Name the blood parasite species.
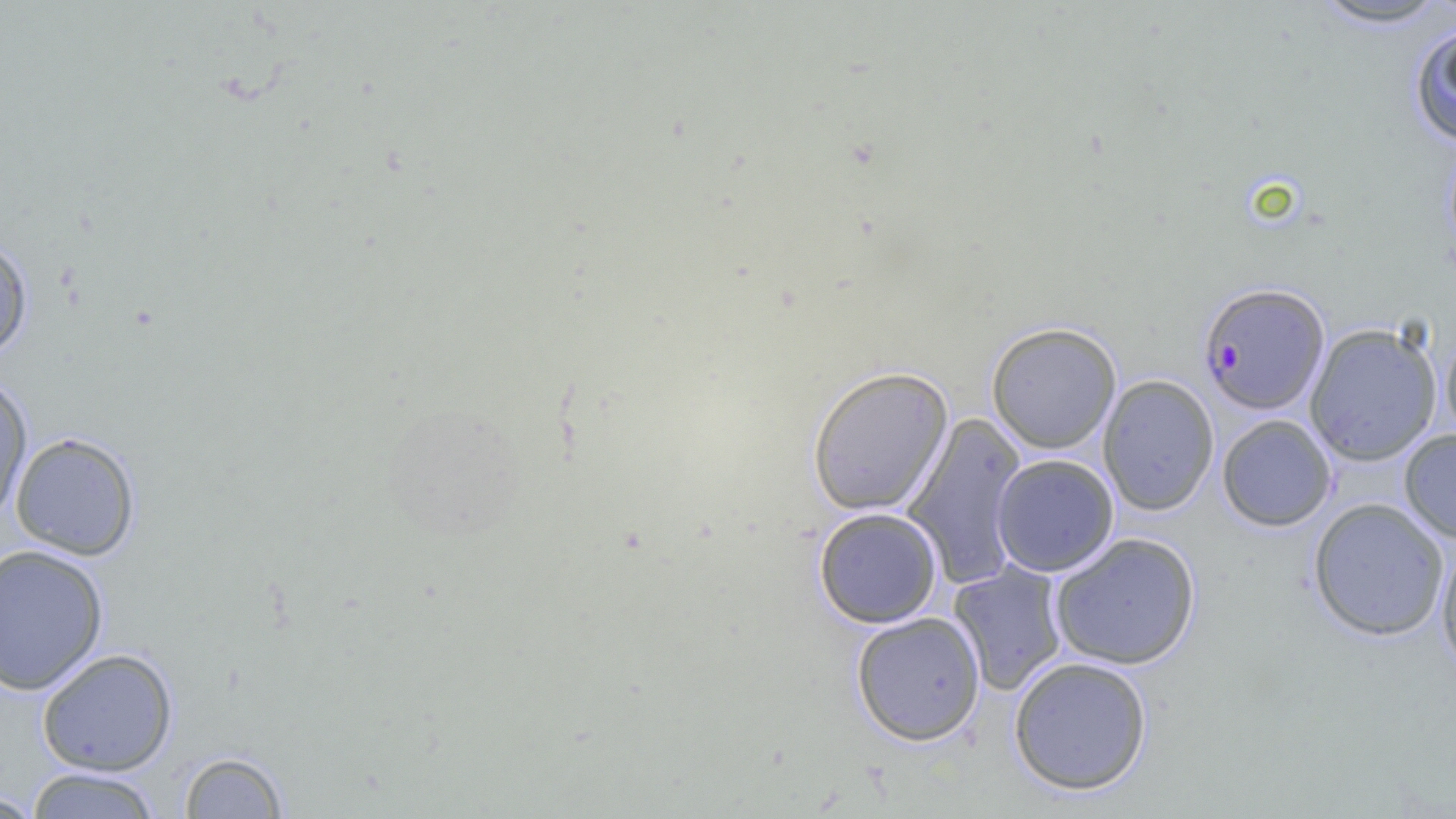
Plasmodium falciparum.

Approximate bounding boxes as [x1, y1, x2, y2] in pixels. Plasmodium falciparum-infected red blood cell locations: [1198, 282, 1330, 415]. Uninfected red blood cell locations: [1308, 0, 1454, 29], [1409, 22, 1456, 147], [0, 233, 34, 362], [986, 322, 1121, 454], [1304, 322, 1442, 466], [1441, 326, 1456, 443], [807, 366, 953, 517], [0, 372, 33, 525], [1098, 374, 1219, 516], [901, 411, 1028, 590], [1217, 414, 1336, 532], [1399, 429, 1456, 543], [10, 432, 141, 561], [991, 454, 1119, 577], [1308, 498, 1450, 641], [813, 506, 943, 629], [1048, 532, 1201, 670], [1435, 541, 1456, 675], [0, 543, 109, 697], [948, 561, 1069, 696], [850, 611, 986, 746], [36, 648, 178, 777], [1008, 656, 1153, 796], [177, 750, 290, 818], [24, 767, 163, 818], [0, 790, 45, 818]. Light microscopy. Image is 1456×819 pixels. One field of a larger specimen. 1000x magnification. Thin blood film.